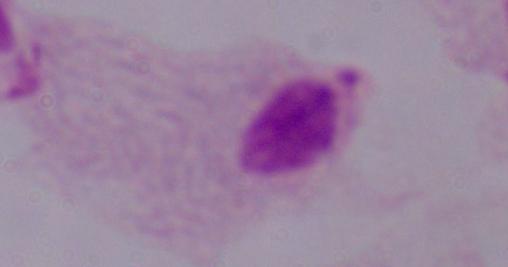

Summary:
  - Magnification: 1000x
  - Modality: photomicrograph
  - Identification: trichomonad